Classify this cell by malaria status.
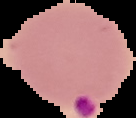
It is parasitized.

Summary:
  - Preparation: thin blood smear
  - Image size: 136×118 pixels
  - Image type: cell region segmented out of the field of view; surrounding area masked to black